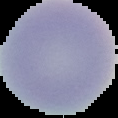

Summary:
  - Image size: 118×118 pixels
  - Image type: cell region segmented out of the field of view; surrounding area masked to black
  - Malaria status: uninfected
  - Preparation: thin blood smear